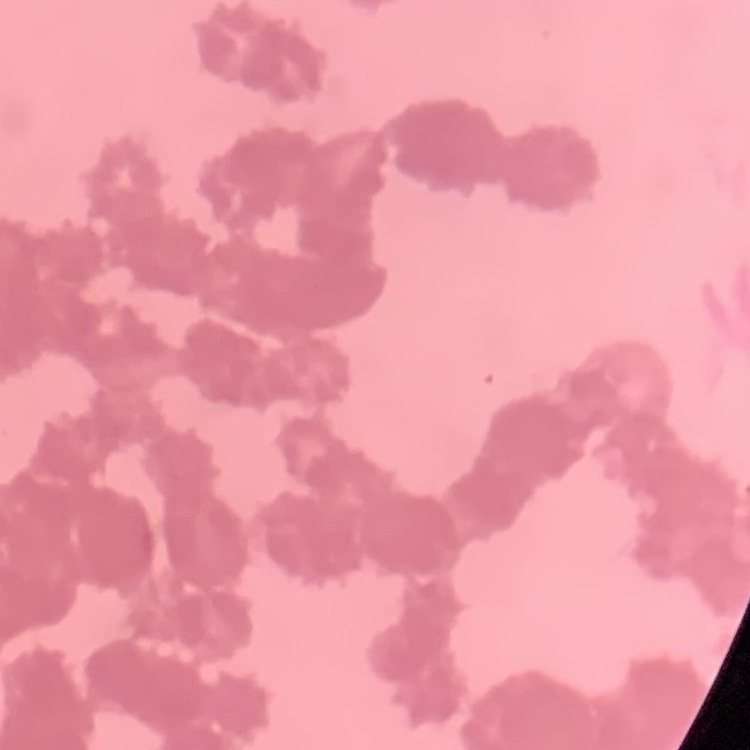
erythrocyte morphology = rouleaux formation
preparation = thin peripheral smear
image type = square crop of a larger photomicrograph
stain = Field's or Giemsa